Identify the parasite.
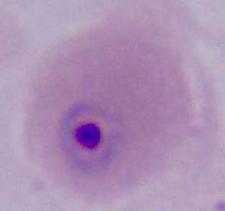
This is Plasmodium.

Captured at either 400x or 1000x magnification. Photomicrograph.